Locate every Plasmodium falciparum-infected red blood cell.
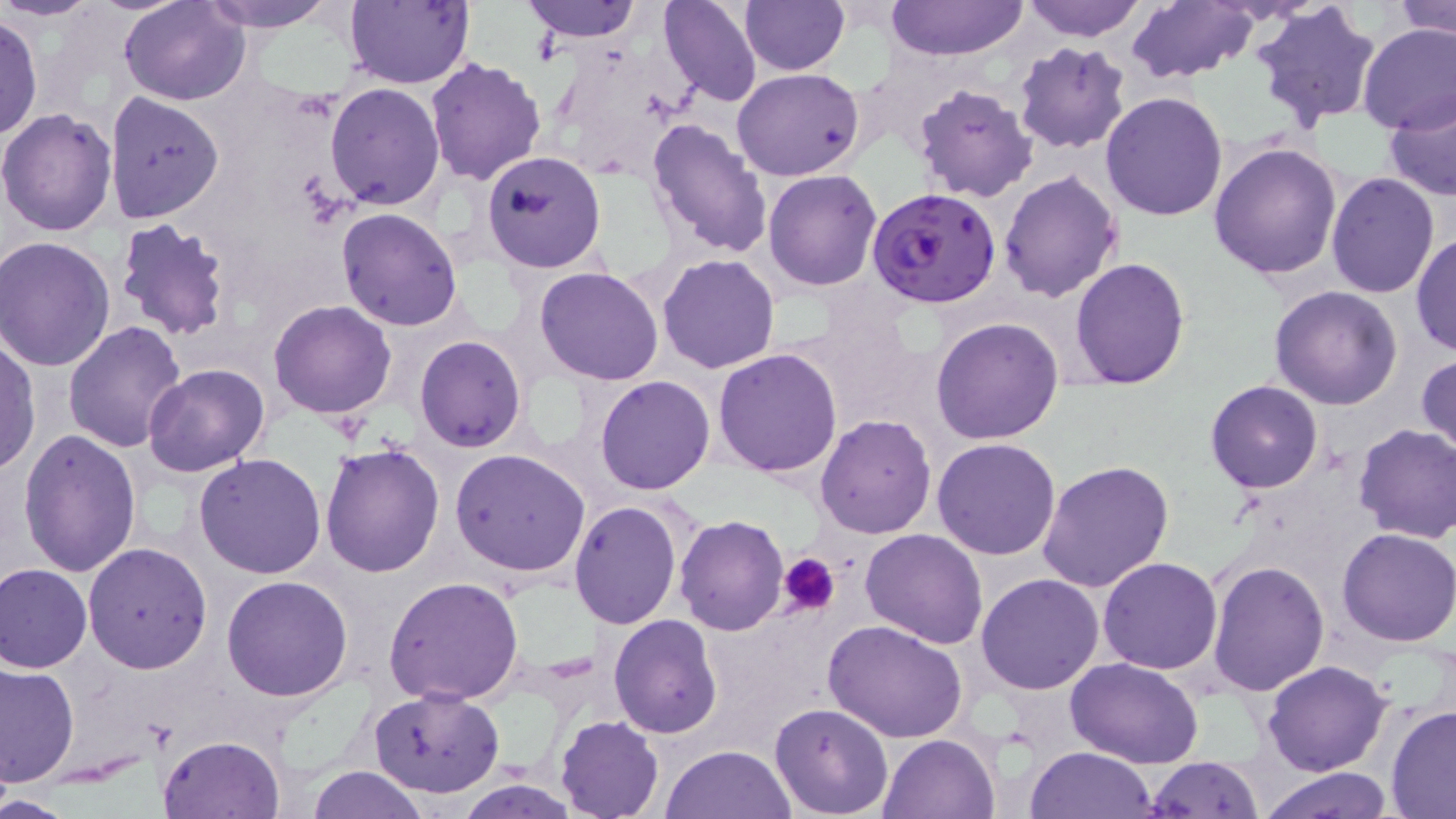
Approximate bounding boxes as (x1,y1)-(x2,y2) corner pairs in pixels.
Plasmodium falciparum-infected red blood cells: (867,188)-(1000,309).

Summary:
  - Platelet locations: (777,552)-(840,617)
  - Uninfected red blood cell locations: (2,0)-(105,21), (120,0)-(251,106), (194,0)-(342,33), (345,0)-(474,89), (522,0)-(643,42), (658,0)-(761,107), (739,0)-(850,75), (1017,0)-(1151,41), (1251,0)-(1383,132), (1391,0)-(1456,40), (885,1)-(1028,63), (1127,1)-(1259,83), (0,13)-(43,142), (1357,23)-(1456,135), (1013,42)-(1132,155), (424,56)-(548,187), (734,66)-(866,180), (325,81)-(447,211), (912,83)-(1040,203), (1383,87)-(1456,203), (104,91)-(224,222), (1100,92)-(1229,222), (0,110)-(118,238), (646,119)-(773,260), (1208,142)-(1343,280), (481,149)-(608,274), (998,169)-(1122,303), (762,170)-(882,291), (1326,171)-(1439,298), (336,208)-(464,331), (115,218)-(233,343), (1413,230)-(1455,360), (2,237)-(117,371), (658,253)-(780,373), (1071,257)-(1190,392), (536,267)-(664,386), (1269,287)-(1404,409), (269,301)-(397,419), (931,316)-(1064,446), (62,320)-(188,452), (415,335)-(526,452), (0,337)-(39,475), (713,349)-(843,479), (1418,352)-(1456,464), (143,364)-(271,478), (595,375)-(715,495), (1205,379)-(1323,494), (815,413)-(937,539), (1353,424)-(1456,544), (18,429)-(142,580), (933,437)-(1061,559), (320,441)-(446,579), (450,448)-(591,577), (195,452)-(327,578), (1037,458)-(1174,593), (569,502)-(682,629), (675,515)-(788,635), (1336,526)-(1456,646), (860,528)-(987,647), (83,543)-(213,672), (1098,557)-(1224,675), (1207,559)-(1329,696), (0,563)-(93,674), (976,572)-(1106,695), (221,575)-(354,701), (384,575)-(526,705), (608,615)-(721,737), (824,619)-(970,743), (1066,658)-(1206,768), (1261,659)-(1393,777), (1,663)-(79,786), (369,685)-(504,799), (770,703)-(894,817), (1385,706)-(1456,817), (555,715)-(664,819), (158,734)-(285,818), (879,734)-(1001,819), (662,745)-(794,819), (1024,747)-(1158,819), (1142,755)-(1266,818), (307,765)-(429,819), (1259,766)-(1395,819), (456,780)-(581,817), (0,792)-(73,818)
  - Slide-level diagnosis: Plasmodium falciparum
  - Modality: light microscopy
  - Preparation: thin blood film
  - Stain: May-Grünwald-Giemsa
  - Field of view: one of a larger specimen
  - Magnification: 1000x
  - Image size: 1456×819 pixels